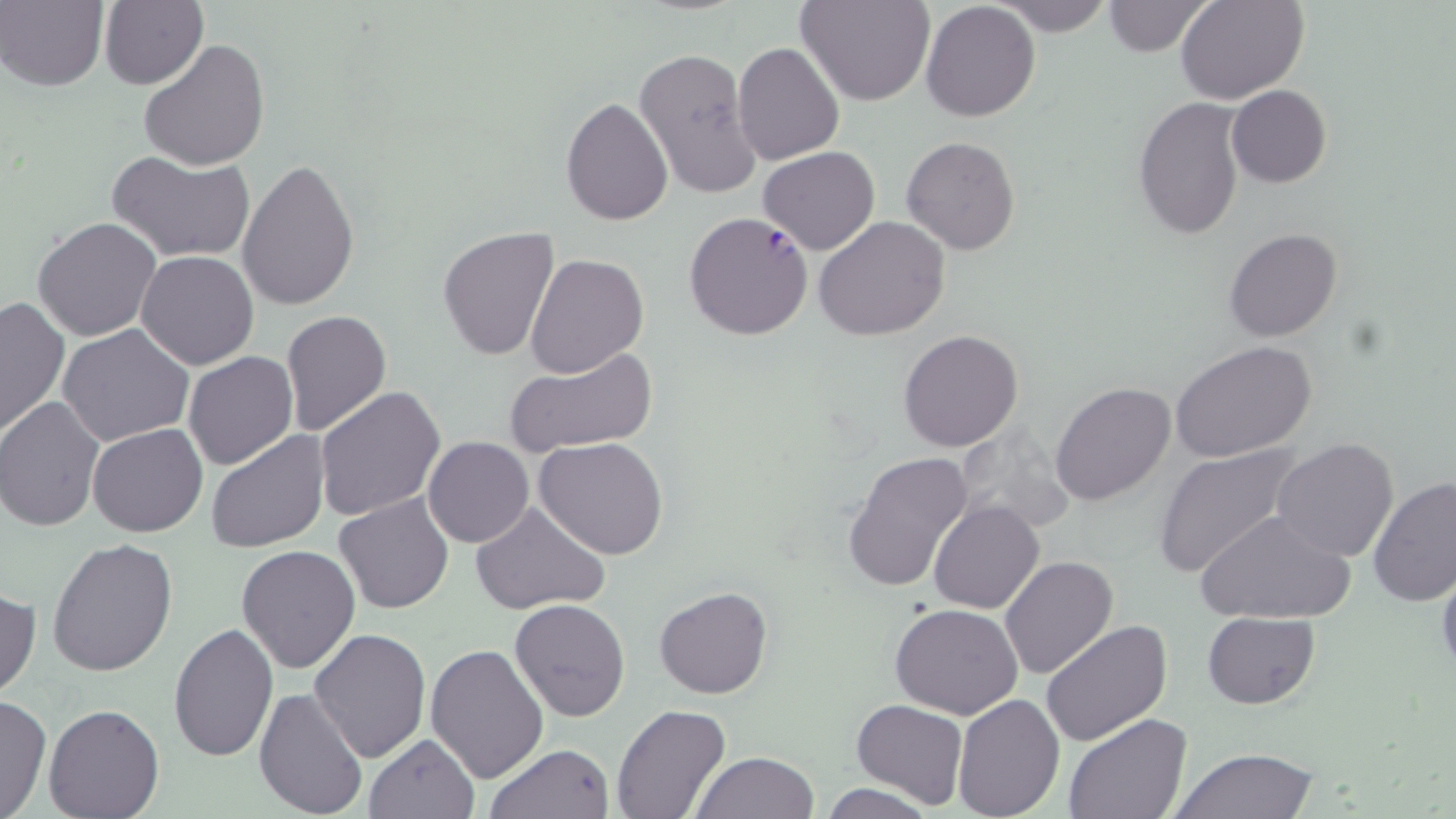

Summary:
  - Coordinate format: approximate bounding boxes as (x1,y1)-(x2,y2) corner pairs in pixels
  - Plasmodium falciparum-infected red blood cell locations: (685,211)-(815,341)
  - Uninfected red blood cell locations: (1,0)-(108,90), (100,0)-(209,90), (798,0)-(933,106), (994,0)-(1117,37), (1101,0)-(1216,57), (1177,0)-(1310,104), (919,1)-(1040,122), (140,39)-(271,171), (732,42)-(846,166), (633,46)-(759,202), (1226,83)-(1331,187), (560,96)-(672,225), (1132,99)-(1246,239), (902,135)-(1020,255), (758,147)-(882,255), (106,148)-(256,265), (236,158)-(361,312), (32,216)-(162,340), (813,216)-(951,339), (437,226)-(559,360), (1225,228)-(1342,342), (136,250)-(258,369), (525,251)-(649,378), (0,294)-(70,436), (280,310)-(392,437), (58,324)-(194,447), (897,328)-(1023,451), (1172,342)-(1318,464), (504,344)-(657,458), (183,351)-(299,470), (1049,382)-(1176,505), (315,386)-(446,523), (0,397)-(104,531), (87,423)-(208,537), (205,429)-(330,553), (423,436)-(533,548), (534,436)-(669,559), (1272,437)-(1400,563), (1152,443)-(1304,579), (842,450)-(973,593), (1368,476)-(1456,607), (334,493)-(455,613), (469,500)-(611,619), (930,501)-(1044,615), (1194,508)-(1357,624), (48,536)-(178,678), (237,544)-(361,673), (1000,555)-(1119,680), (1436,562)-(1456,681), (0,585)-(41,700), (654,585)-(772,699), (509,599)-(632,720), (890,601)-(1023,717), (1203,610)-(1319,709), (169,621)-(279,762), (1040,621)-(1170,747), (309,628)-(432,762), (425,642)-(548,782), (254,687)-(370,819), (950,694)-(1065,818), (0,695)-(51,819), (851,699)-(969,809), (44,703)-(164,819), (610,705)-(731,819), (1062,713)-(1191,819), (364,733)-(479,818), (484,742)-(616,818), (1170,745)-(1321,818), (691,751)-(821,819), (818,783)-(936,819)
  - Slide-level diagnosis: Plasmodium falciparum
  - Preparation: thin blood smear
  - Stain: May-Grünwald-Giemsa
  - Magnification: 1000x
  - Field of view: one of a larger specimen
  - Modality: optical microscopy
  - Image size: 1456×819 pixels